Assess this cell for malaria.
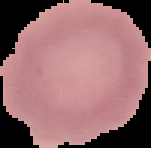
It is uninfected.

Summary:
  - Preparation: thin blood smear
  - Image size: 151×148 pixels
  - Image type: segmented cell region on a black background